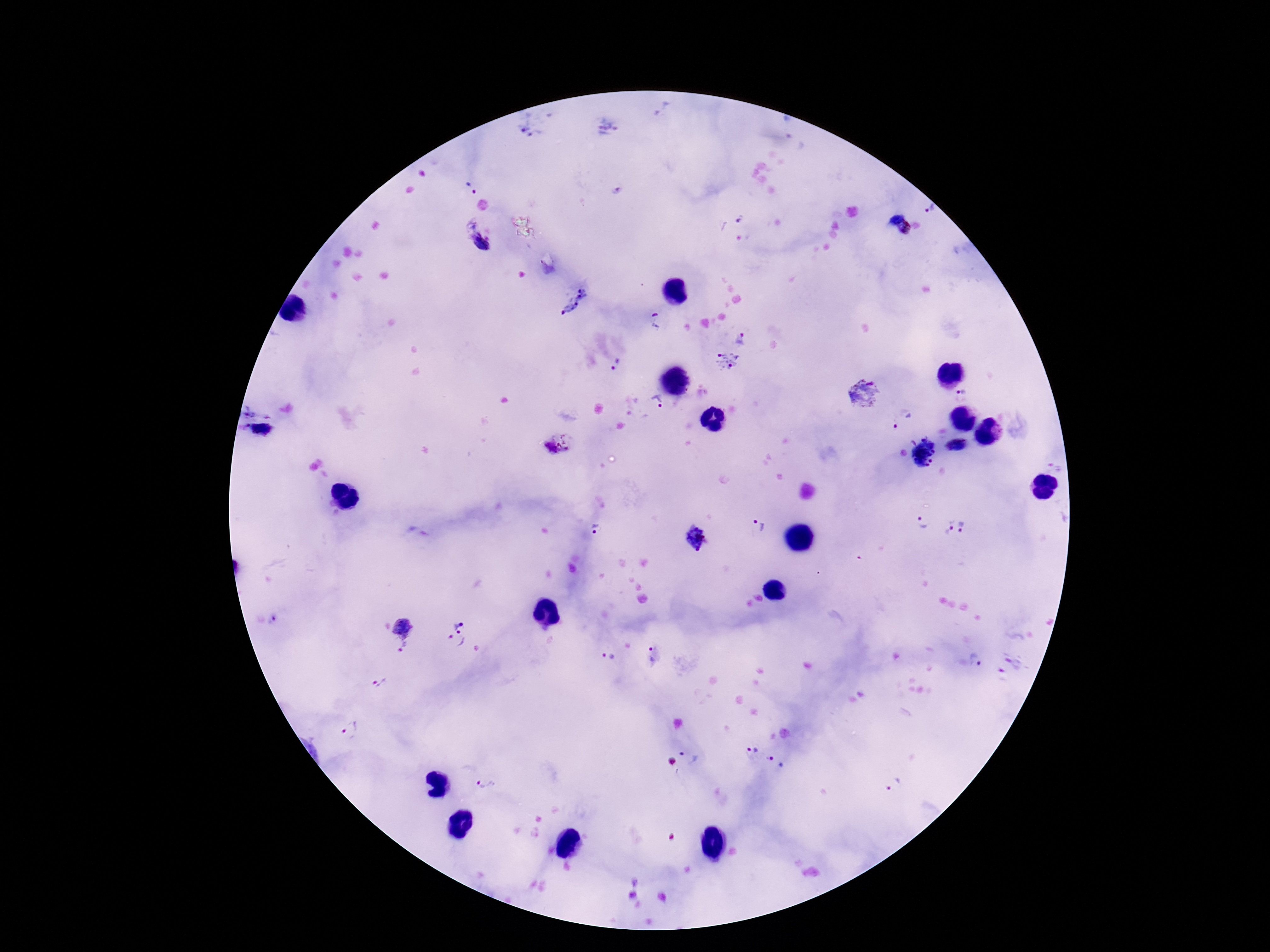
capture: smartphone camera through the microscope eyepiece
stain: Giemsa
image_size: 1270×952 pixels
magnification: 100x
field_of_view: one from this slide
preparation: thick blood smear
plasmodium_parasite_locations: 'approximate centers as [x, y] in pixels: [608, 128], [527, 130], [471, 188], [930, 208], [894, 216], [741, 220], [905, 229], [481, 242], [575, 300], [657, 321], [742, 338], [727, 361], [617, 365], [865, 394], [963, 396], [658, 400], [263, 431], [555, 442], [956, 446], [923, 452], [1057, 465], [922, 522], [760, 526], [947, 527], [965, 527], [596, 528], [695, 539], [402, 625], [455, 633], [403, 646], [652, 655], [608, 657], [976, 661], [379, 683], [351, 730], [753, 748], [692, 756], [672, 761], [777, 761], [483, 783], [893, 785]'
patient_malaria_status: infected